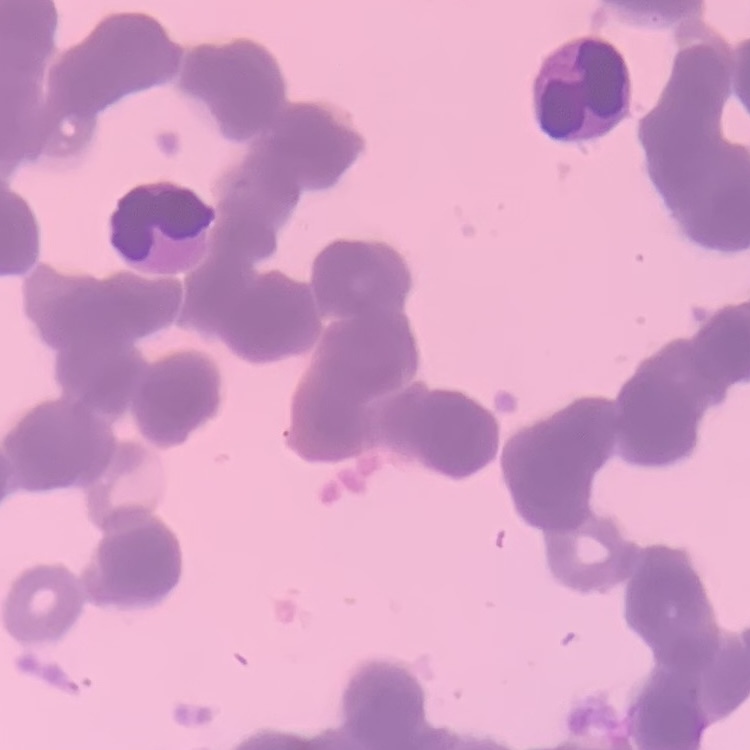

Summary:
  - Erythrocyte morphology: rouleaux formation
  - Stain: Field's or Giemsa
  - Image type: one tile cut from a larger photomicrograph
  - Preparation: thin blood smear